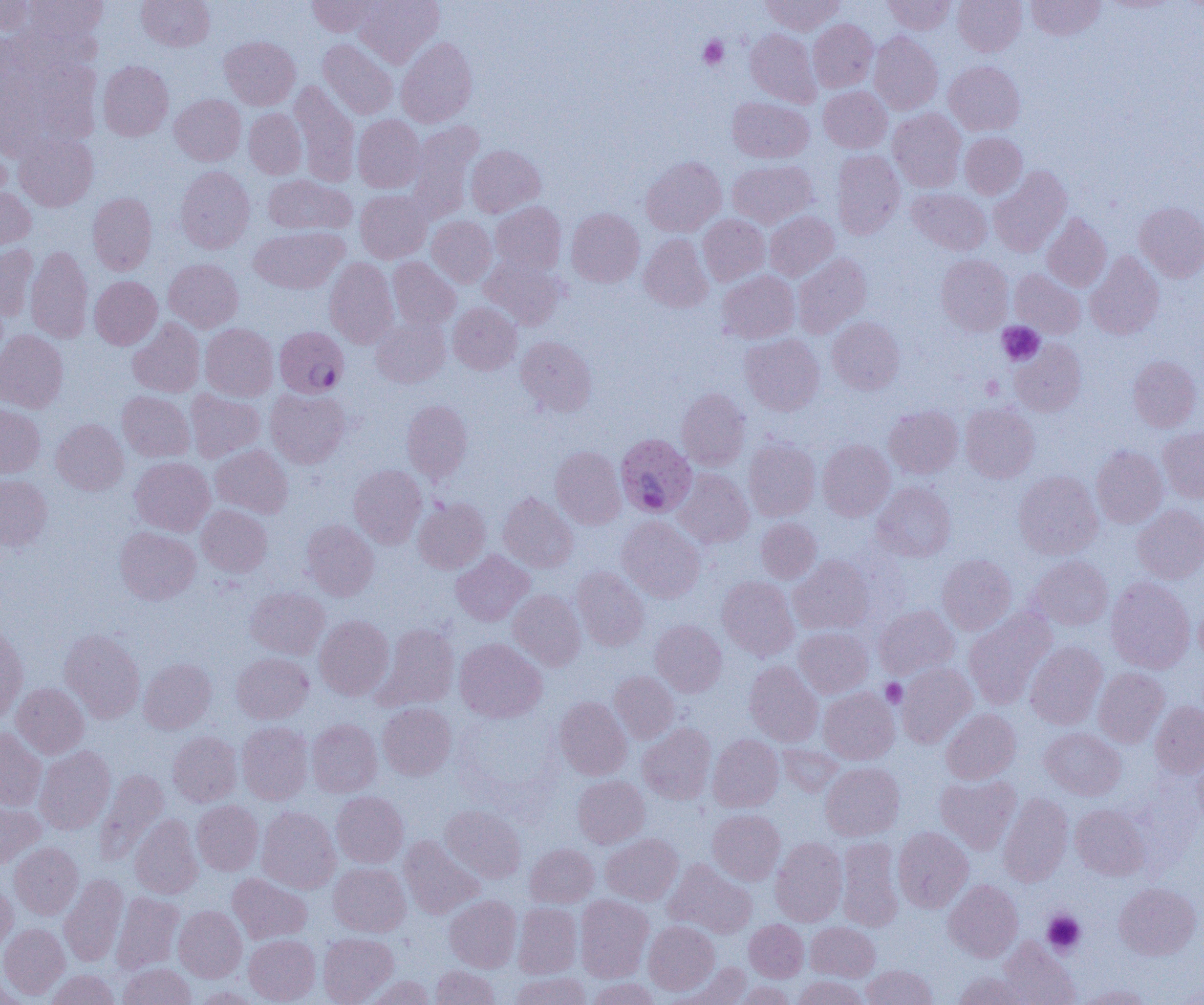

Approximate bounding boxes as (x1,y1)-(x2,y2) corner pairs in pixels. Uninfected red blood cell locations: (0,0)-(36,35), (25,0)-(107,43), (137,0)-(214,51), (307,0)-(381,37), (355,0)-(444,67), (761,0)-(844,35), (882,0)-(955,34), (953,0)-(1026,56), (1026,0)-(1106,40), (808,19)-(878,92), (0,29)-(18,95), (745,29)-(821,107), (868,31)-(942,115), (219,36)-(300,110), (396,37)-(477,127), (318,39)-(397,120), (17,55)-(103,152), (98,60)-(173,140), (944,61)-(1025,135), (289,81)-(360,186), (819,86)-(892,152), (169,94)-(246,165), (727,97)-(814,163), (243,108)-(307,179), (888,108)-(966,192), (353,115)-(425,192), (406,122)-(482,222), (13,132)-(98,211), (960,132)-(1027,199), (0,142)-(10,208), (466,145)-(545,217), (831,150)-(905,239), (641,156)-(726,236), (728,160)-(817,228), (176,166)-(255,253), (989,166)-(1071,257), (263,174)-(356,236), (0,186)-(35,250), (907,188)-(991,255), (355,190)-(431,262), (87,192)-(157,275), (491,202)-(566,275), (1134,202)-(1204,281), (566,208)-(644,287), (765,211)-(839,281), (698,214)-(769,285), (1042,214)-(1111,291), (427,216)-(497,287), (249,226)-(348,293), (639,233)-(713,312), (0,244)-(39,320), (26,245)-(93,343), (1085,251)-(1164,340), (793,253)-(871,338), (936,254)-(1013,335), (481,255)-(565,330), (387,257)-(460,331), (164,258)-(243,332), (324,258)-(399,348), (1010,269)-(1086,338), (717,271)-(800,343), (89,276)-(162,349), (448,302)-(522,374), (827,316)-(905,394), (128,318)-(205,397), (371,318)-(450,387), (200,323)-(278,401), (0,330)-(68,412), (740,333)-(825,415), (516,336)-(597,417), (1010,339)-(1086,416), (1128,356)-(1202,431), (265,387)-(350,468), (185,389)-(265,462), (677,389)-(750,470), (117,391)-(195,462), (401,400)-(472,483), (960,403)-(1040,482), (0,404)-(45,478), (884,405)-(963,478), (51,419)-(128,495), (1158,427)-(1204,503), (744,439)-(820,521), (817,439)-(895,521), (210,444)-(293,518), (550,446)-(626,528), (1091,446)-(1167,528), (130,457)-(215,536), (348,464)-(427,548), (674,469)-(753,548), (1013,471)-(1102,559), (0,475)-(52,551), (872,482)-(956,562), (498,493)-(578,572), (413,497)-(490,573), (197,504)-(272,577), (1132,504)-(1204,583), (616,516)-(705,602), (756,518)-(821,583), (301,520)-(378,601), (115,526)-(200,604), (451,550)-(534,626), (937,554)-(1016,634), (789,556)-(875,634), (1029,556)-(1113,630), (572,567)-(649,651), (717,576)-(799,660), (1106,577)-(1195,673), (245,588)-(329,659), (508,590)-(586,670), (874,605)-(958,679), (1195,605)-(1204,663), (963,609)-(1057,709), (315,615)-(394,700), (650,619)-(727,696), (0,623)-(28,722), (373,623)-(459,711), (794,627)-(873,698), (60,628)-(145,723), (454,638)-(546,723), (1025,641)-(1107,729), (232,652)-(313,723), (138,658)-(216,733), (744,661)-(823,747), (896,663)-(976,747), (1093,667)-(1169,747), (609,671)-(679,743), (11,683)-(88,758), (819,687)-(899,764), (554,696)-(632,780), (1150,701)-(1204,778), (377,703)-(456,780), (941,708)-(1021,784), (307,719)-(382,797), (237,721)-(313,804), (638,723)-(716,804), (1039,727)-(1126,800), (0,728)-(47,810), (168,731)-(241,806), (708,735)-(783,812), (777,743)-(843,796), (34,746)-(115,834), (1193,750)-(1204,831), (820,762)-(904,840), (96,769)-(169,863), (936,775)-(1021,853), (573,776)-(649,848), (331,791)-(408,868), (998,793)-(1073,886), (0,800)-(45,867), (191,800)-(263,875), (1070,804)-(1151,880), (440,805)-(526,882), (257,806)-(340,893), (708,810)-(785,884), (130,814)-(202,899), (893,827)-(973,912), (601,834)-(682,905), (399,836)-(483,919), (771,837)-(847,926), (837,837)-(903,930), (10,843)-(83,919), (525,843)-(598,907), (664,859)-(756,939), (329,863)-(410,936), (227,873)-(312,944), (59,874)-(128,967), (943,880)-(1023,962), (0,881)-(17,955), (1114,883)-(1201,960), (112,892)-(184,974), (445,895)-(521,972), (575,895)-(654,982), (513,903)-(582,978), (173,905)-(247,982), (745,919)-(808,981), (644,920)-(719,994), (806,922)-(880,981), (0,924)-(69,999), (318,932)-(399,1004), (244,934)-(320,1004), (998,938)-(1080,1005), (118,962)-(195,1005), (672,962)-(752,1004), (861,964)-(938,1005), (431,965)-(499,1005), (46,970)-(120,1005), (509,972)-(591,1005), (953,972)-(1029,1005), (0,975)-(21,1005), (361,975)-(436,1005), (792,975)-(868,1005), (587,978)-(660,1005), (733,981)-(795,1005), (1077,984)-(1155,1005), (194,986)-(263,1005). Plasmodium falciparum-infected red blood cell locations: (273,330)-(351,400), (615,433)-(697,517). Platelet locations: (699,36)-(728,69), (997,322)-(1044,366), (981,375)-(1004,399), (881,679)-(907,708), (1042,910)-(1085,955). Slide-level diagnosis: Plasmodium falciparum. One field of a larger specimen. Image is 1204×1005 pixels. Thin blood film. Captured at 1000x magnification. Light microscopy.